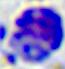
modality: photomicrograph
identification: white blood cell
magnification: 400x